Describe the morphology of the red blood cells.
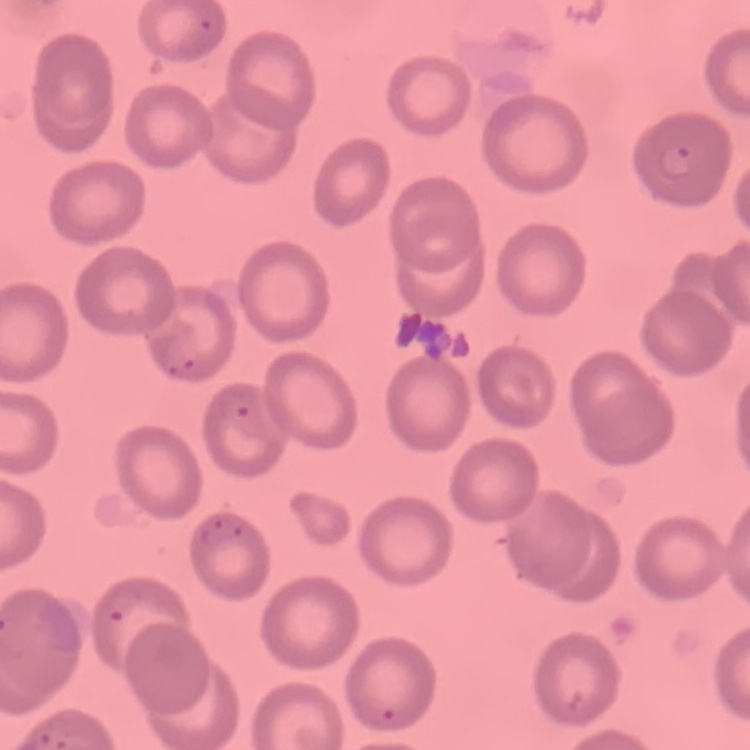
No rouleaux formation.

Summary:
  - Image type: square crop of a larger photomicrograph
  - Preparation: thin blood film
  - Stain: Field's or Giemsa